Report the malaria status of this cell.
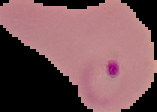
It is parasitized.

Summary:
  - Image size: 157×112 pixels
  - Image type: cell region segmented out of the field of view; surrounding area masked to black
  - Preparation: thin blood film